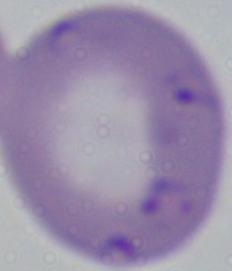
Micrograph. Captured at 1000x magnification. A Babesia parasite is seen.